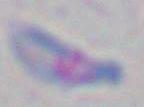 Toxoplasma gondii is seen. Captured at 1000x magnification. Photomicrograph.